Assess this cell for malaria.
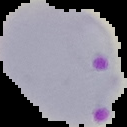
Parasitized.

Summary:
  - Image size: 127×127 pixels
  - Image type: segmented cell region on a black background
  - Preparation: thin blood smear